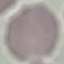
malaria status = uninfected
image type = cell patch, automatically extracted from a larger field of view and resized to 64 × 64 pixels
preparation = thin blood smear
stain = Giemsa
capture = smartphone through the microscope eyepiece